Assess this cell for malaria.
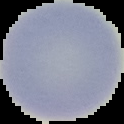

Uninfected.

Summary:
  - Image type: cell region segmented out of the field of view; surrounding area masked to black
  - Preparation: thin blood film
  - Image size: 124×124 pixels